Report the malaria status of this cell.
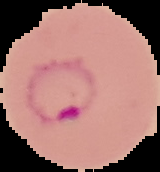

It is parasitized.

Summary:
  - Image type: segmented cell region with the area outside set to black
  - Preparation: thin blood smear
  - Image size: 160×172 pixels